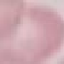

{
  "malaria_status": "uninfected",
  "image_type": "cell patch, automatically extracted from a larger field of view and resized to 64 × 64 pixels",
  "stain": "Giemsa",
  "capture": "smartphone through the microscope eyepiece",
  "preparation": "thin blood smear"
}